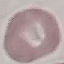

result = no malaria parasites seen
preparation = thin blood film
capture = smartphone through the microscope eyepiece
stain = Giemsa
image type = cell patch, automatically extracted from a larger field of view and resized to 64 × 64 pixels